Locate every leukocyte (white blood cell).
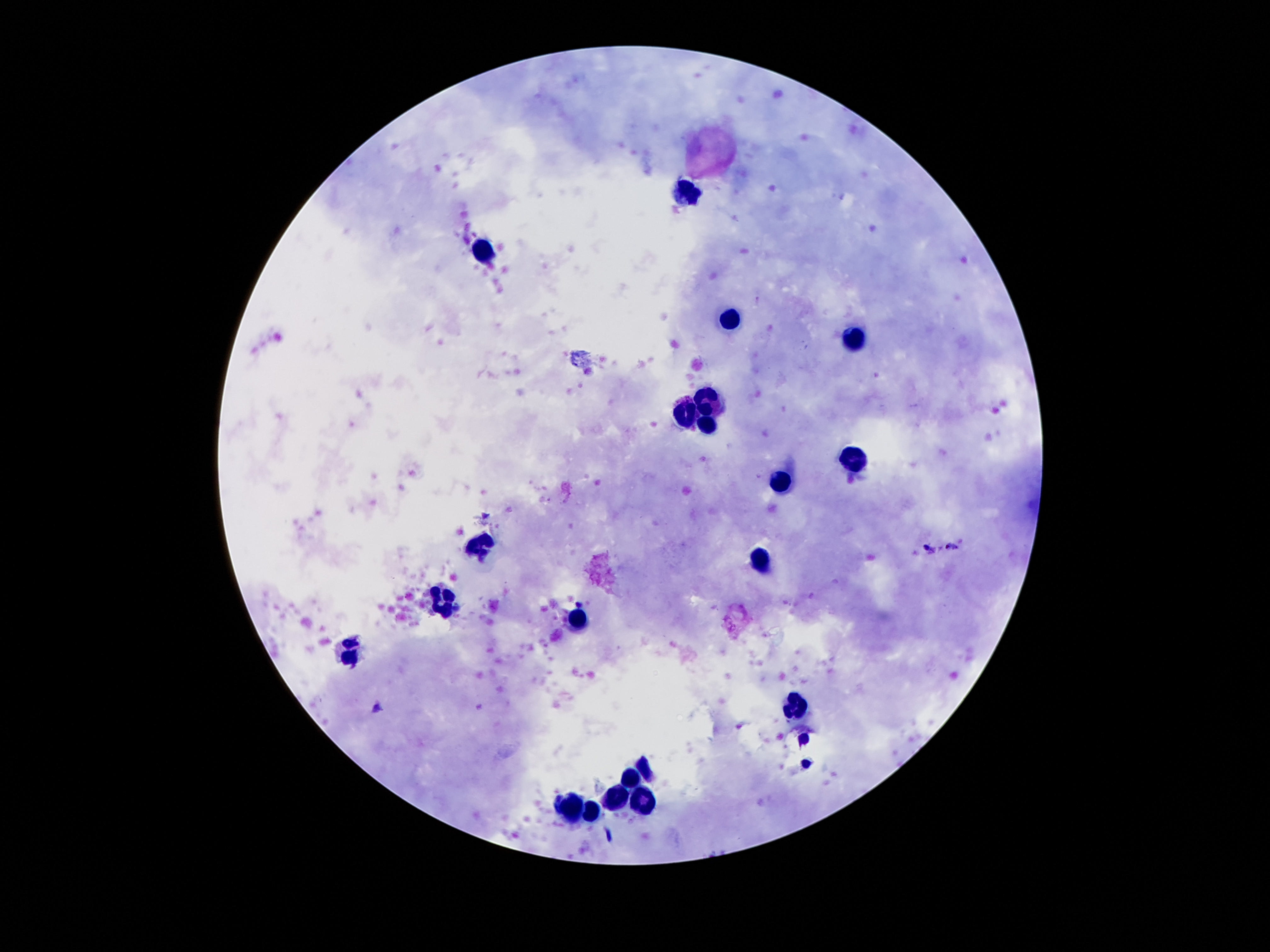
Approximate centers as {x, y} in pixels.
Leukocytes: {687, 192}, {481, 251}, {729, 318}, {853, 341}, {712, 396}, {685, 414}, {708, 423}, {851, 461}, {779, 482}, {479, 541}, {761, 561}, {444, 600}, {576, 618}, {347, 653}, {796, 710}, {631, 779}, {618, 799}, {643, 800}, {570, 809}, {591, 813}.

{
  "magnification": "100x",
  "stain": "Giemsa",
  "field_of_view": "single",
  "image_size": "1270×952 pixels",
  "preparation": "thick peripheral-blood smear",
  "patient_malaria_status": "negative",
  "capture": "smartphone camera through the microscope eyepiece"
}